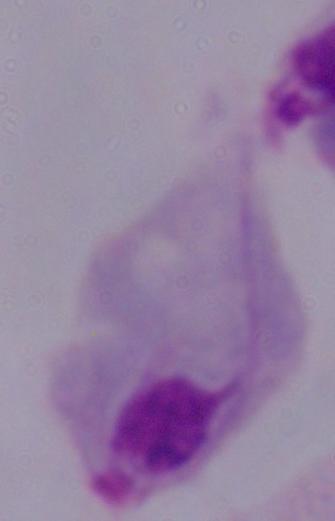

magnification = 1000x
identification = trichomonad
modality = photomicrograph